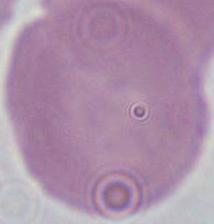

{
  "modality": "photomicrograph",
  "identification": "erythrocyte",
  "magnification": "1000x"
}